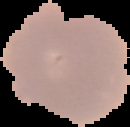

result = no malaria parasites detected
preparation = thin blood film
image size = 130×127 pixels
image type = segmented cell region with the area outside set to black